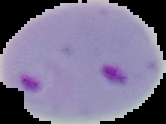

Summary:
  - Preparation: thin blood film
  - Image type: cell region segmented out of the field of view; surrounding area masked to black
  - Malaria status: parasitized
  - Image size: 166×124 pixels